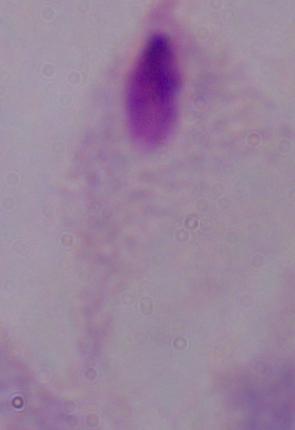

1000x magnification. Photomicrograph. A trichomonad is shown.